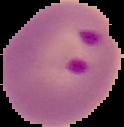
result = malaria parasites detected
preparation = thin blood smear
image size = 124×127 pixels
image type = cell region segmented out of the field of view; surrounding area masked to black